Name the cell type shown.
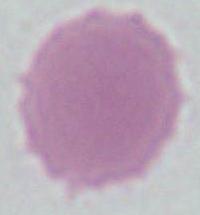
An erythrocyte.

Summary:
  - Magnification: 1000x
  - Modality: micrograph